Report the malaria status of this cell.
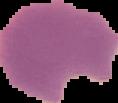

It is parasitized.

image type = segmented cell region with the area outside set to black
preparation = thin blood film
image size = 118×103 pixels